State which parasite is depicted.
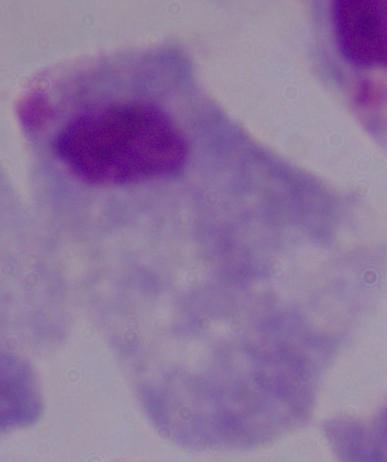
A trichomonad.

Summary:
  - Magnification: 1000x
  - Modality: photomicrograph